Outline each blood parasite and name the species.
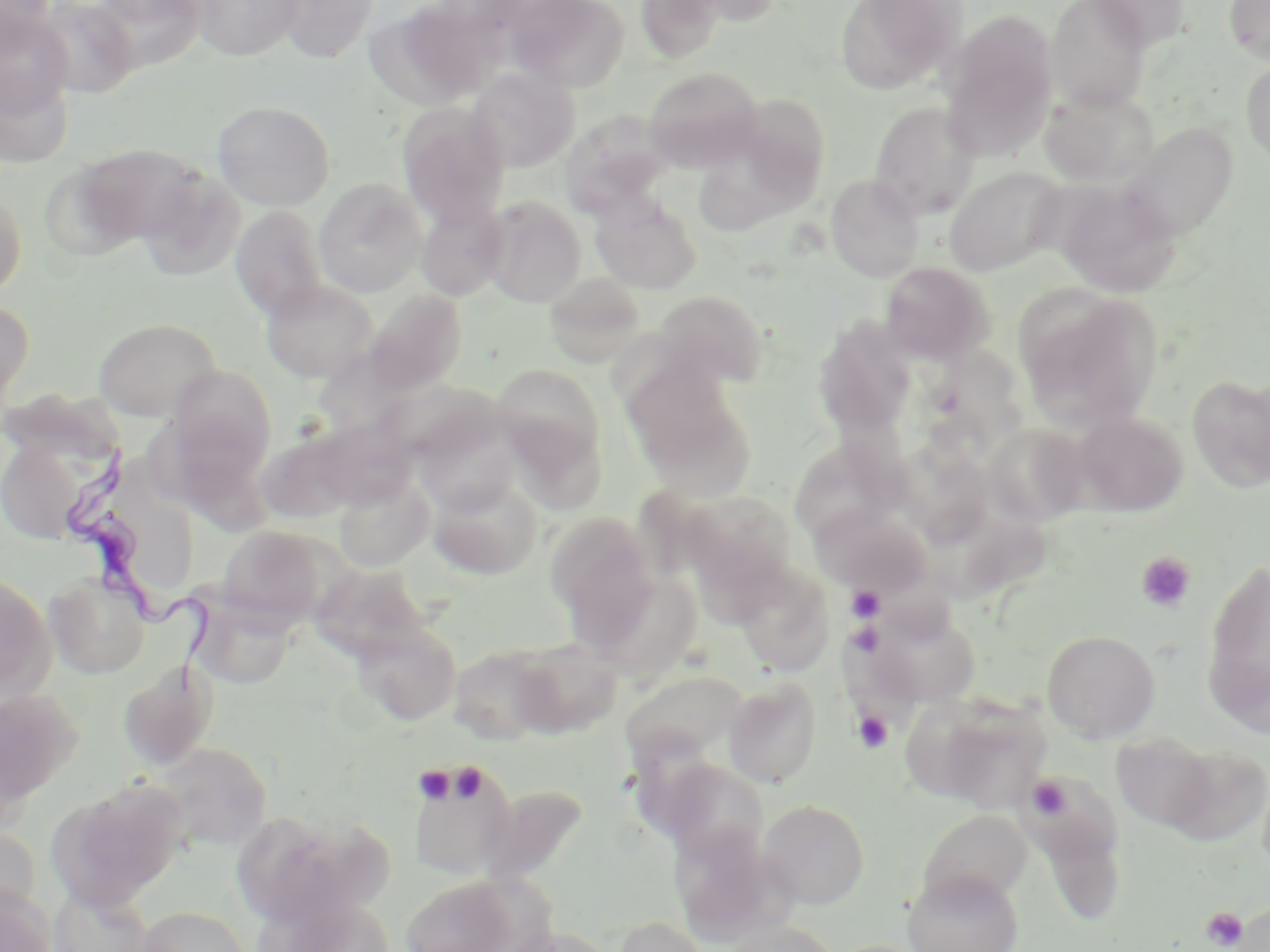

Approximate bounding boxes as named x1/y1/x2/y2 corners in pixels.
Trypanosoma brucei: (x1=63, y1=436, x2=220, y2=697).
No Plasmodium falciparum, Plasmodium ovale, Plasmodium malariae, Plasmodium vivax, or Babesia divergens observed.

Uninfected red blood cell locations: (x1=0, y1=0, x2=58, y2=52), (x1=32, y1=0, x2=141, y2=99), (x1=92, y1=0, x2=209, y2=73), (x1=191, y1=0, x2=305, y2=61), (x1=276, y1=0, x2=381, y2=64), (x1=374, y1=0, x2=505, y2=109), (x1=508, y1=0, x2=629, y2=91), (x1=634, y1=0, x2=725, y2=64), (x1=672, y1=0, x2=786, y2=27), (x1=835, y1=0, x2=959, y2=93), (x1=1046, y1=0, x2=1150, y2=109), (x1=1087, y1=0, x2=1190, y2=52), (x1=1224, y1=0, x2=1270, y2=64), (x1=0, y1=7, x2=75, y2=123), (x1=940, y1=13, x2=1059, y2=162), (x1=1241, y1=59, x2=1270, y2=167), (x1=643, y1=67, x2=763, y2=172), (x1=466, y1=68, x2=579, y2=172), (x1=1038, y1=86, x2=1159, y2=189), (x1=732, y1=94, x2=831, y2=204), (x1=212, y1=100, x2=336, y2=211), (x1=869, y1=101, x2=981, y2=219), (x1=397, y1=103, x2=510, y2=228), (x1=563, y1=112, x2=670, y2=218), (x1=1123, y1=123, x2=1238, y2=241), (x1=67, y1=143, x2=204, y2=251), (x1=698, y1=158, x2=801, y2=238), (x1=945, y1=166, x2=1067, y2=276), (x1=136, y1=167, x2=246, y2=280), (x1=826, y1=174, x2=925, y2=282), (x1=313, y1=178, x2=427, y2=297), (x1=1055, y1=182, x2=1180, y2=297), (x1=0, y1=189, x2=27, y2=300), (x1=592, y1=195, x2=702, y2=294), (x1=479, y1=196, x2=587, y2=307), (x1=415, y1=199, x2=509, y2=301), (x1=230, y1=205, x2=329, y2=320), (x1=880, y1=262, x2=994, y2=365), (x1=543, y1=273, x2=647, y2=367), (x1=260, y1=278, x2=378, y2=383), (x1=1018, y1=288, x2=1162, y2=433), (x1=360, y1=290, x2=467, y2=398), (x1=651, y1=290, x2=768, y2=389), (x1=0, y1=300, x2=34, y2=418), (x1=816, y1=315, x2=921, y2=435), (x1=93, y1=318, x2=222, y2=421), (x1=924, y1=335, x2=1036, y2=462), (x1=494, y1=364, x2=604, y2=475), (x1=165, y1=365, x2=277, y2=479), (x1=623, y1=365, x2=756, y2=499), (x1=1187, y1=374, x2=1270, y2=493), (x1=381, y1=378, x2=504, y2=464), (x1=414, y1=411, x2=522, y2=515), (x1=1072, y1=412, x2=1188, y2=516), (x1=299, y1=417, x2=421, y2=512), (x1=982, y1=422, x2=1091, y2=528), (x1=257, y1=425, x2=369, y2=524), (x1=0, y1=436, x2=95, y2=547), (x1=795, y1=439, x2=921, y2=528), (x1=901, y1=439, x2=1004, y2=551), (x1=334, y1=472, x2=434, y2=572), (x1=426, y1=475, x2=543, y2=579), (x1=680, y1=493, x2=798, y2=607), (x1=814, y1=505, x2=931, y2=597), (x1=544, y1=511, x2=662, y2=642), (x1=216, y1=525, x2=332, y2=627), (x1=1203, y1=557, x2=1270, y2=728), (x1=731, y1=560, x2=835, y2=675), (x1=309, y1=563, x2=431, y2=662), (x1=0, y1=571, x2=56, y2=701), (x1=44, y1=572, x2=151, y2=678), (x1=623, y1=582, x2=706, y2=694), (x1=191, y1=595, x2=296, y2=689), (x1=861, y1=601, x2=984, y2=711), (x1=349, y1=620, x2=461, y2=726), (x1=1042, y1=629, x2=1161, y2=742), (x1=508, y1=638, x2=622, y2=738), (x1=449, y1=642, x2=565, y2=744), (x1=117, y1=660, x2=219, y2=771), (x1=723, y1=677, x2=822, y2=788), (x1=629, y1=680, x2=758, y2=772), (x1=0, y1=687, x2=83, y2=810), (x1=917, y1=694, x2=1051, y2=811), (x1=155, y1=742, x2=272, y2=852), (x1=1156, y1=743, x2=1269, y2=847), (x1=408, y1=758, x2=517, y2=880), (x1=1022, y1=760, x2=1133, y2=927), (x1=661, y1=766, x2=770, y2=872), (x1=49, y1=779, x2=188, y2=912), (x1=483, y1=786, x2=586, y2=880), (x1=759, y1=799, x2=870, y2=908), (x1=918, y1=808, x2=1034, y2=909), (x1=233, y1=809, x2=391, y2=931), (x1=671, y1=823, x2=788, y2=943), (x1=0, y1=825, x2=41, y2=921), (x1=902, y1=868, x2=1024, y2=952), (x1=399, y1=877, x2=521, y2=951), (x1=48, y1=885, x2=157, y2=952), (x1=0, y1=886, x2=57, y2=952), (x1=269, y1=896, x2=400, y2=951), (x1=1227, y1=900, x2=1270, y2=952), (x1=136, y1=904, x2=254, y2=952), (x1=610, y1=915, x2=714, y2=952), (x1=718, y1=920, x2=841, y2=952), (x1=494, y1=925, x2=619, y2=952). Platelet locations: (x1=1137, y1=551, x2=1196, y2=612), (x1=847, y1=585, x2=886, y2=623), (x1=852, y1=711, x2=894, y2=755), (x1=454, y1=763, x2=492, y2=811), (x1=413, y1=764, x2=457, y2=804), (x1=1026, y1=776, x2=1072, y2=821), (x1=1201, y1=906, x2=1249, y2=950). Slide-level diagnosis: Trypanosoma brucei. Captured at 1000x magnification. May-Grünwald-Giemsa stain. Image is 1270×952 pixels. Thin blood film. Optical microscopy. One field of a larger specimen.